Classify this cell by malaria status.
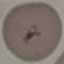

It is uninfected.

{
  "stain": "Giemsa",
  "preparation": "thin smear",
  "image_type": "automatically extracted cell patch, resized to 64 × 64 pixels",
  "capture": "smartphone camera at the microscope eyepiece"
}